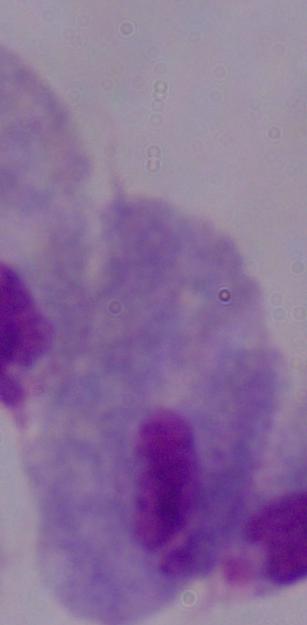
magnification = 1000x
modality = photomicrograph
identification = trichomonad